Classify this cell by malaria status.
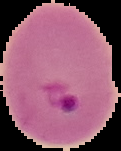
It is parasitized.

{
  "image_size": "121×151 pixels",
  "image_type": "cell region segmented out of the field of view; surrounding area masked to black",
  "preparation": "thin blood film"
}